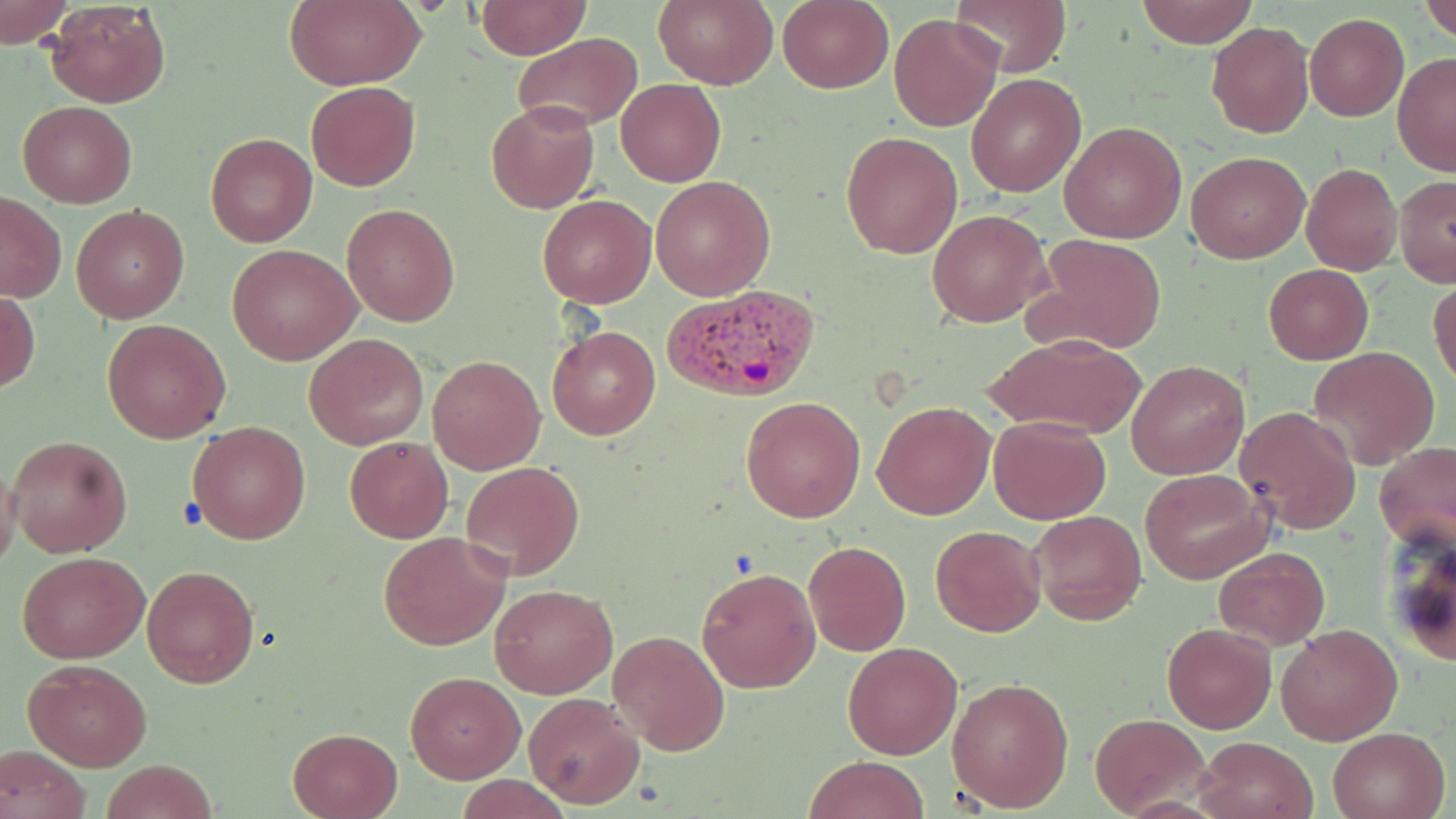
slide-level diagnosis = Plasmodium vivax
field of view = one of a larger specimen
stain = May-Grünwald-Giemsa
image size = 1456×819 pixels
uninfected red blood cell locations = approximate bounding boxes as (x1,y1)-(x2,y2) corner pairs in pixels: (0,0)-(75,47), (284,0)-(426,90), (474,0)-(589,58), (654,0)-(778,88), (948,0)-(1071,76), (1135,0)-(1259,47), (1418,0)-(1456,44), (44,1)-(171,109), (778,1)-(893,93), (889,13)-(1003,133), (1305,13)-(1409,121), (1207,21)-(1313,138), (513,34)-(641,132), (1392,52)-(1456,176), (966,74)-(1086,196), (616,78)-(726,187), (305,81)-(420,192), (16,101)-(137,208), (485,101)-(599,214), (1059,121)-(1186,244), (842,131)-(963,259), (205,132)-(317,246), (1185,151)-(1310,263), (1302,163)-(1402,275), (1394,174)-(1456,288), (651,175)-(776,300), (0,192)-(67,302), (536,194)-(655,308), (342,202)-(460,327), (72,204)-(189,322), (926,209)-(1052,328), (1028,234)-(1168,355), (228,243)-(362,365), (1262,264)-(1374,364), (1429,277)-(1456,389), (1,290)-(40,395), (102,319)-(232,443), (547,324)-(660,441), (304,332)-(429,449), (981,332)-(1148,440), (1307,345)-(1441,469), (429,355)-(545,473), (1126,359)-(1250,480), (740,395)-(866,523), (872,401)-(995,520), (1235,406)-(1361,533), (988,416)-(1112,524), (187,420)-(311,545), (6,435)-(133,556), (344,435)-(454,543), (1375,439)-(1456,557), (460,460)-(585,580), (0,461)-(23,567), (1140,469)-(1273,584), (1028,510)-(1146,627), (931,525)-(1044,638), (1381,525)-(1456,668), (376,531)-(512,650), (802,539)-(912,655), (1212,546)-(1329,650), (18,551)-(149,662), (141,565)-(260,688), (696,566)-(821,694), (489,583)-(617,699), (1161,623)-(1277,734), (1275,624)-(1403,745), (610,629)-(729,754), (842,641)-(962,759), (23,657)-(151,770), (404,671)-(524,782), (946,677)-(1076,812), (522,691)-(645,809), (1091,712)-(1210,816), (1327,725)-(1452,819), (288,727)-(402,818), (1195,735)-(1317,819), (0,745)-(90,819), (803,754)-(931,818), (100,759)-(218,819), (455,776)-(573,817)
modality = light microscopy
magnification = 1000x
preparation = thin blood smear
Plasmodium vivax-infected red blood cell locations = approximate bounding boxes as (x1,y1)-(x2,y2) corner pairs in pixels: (660,284)-(822,403)